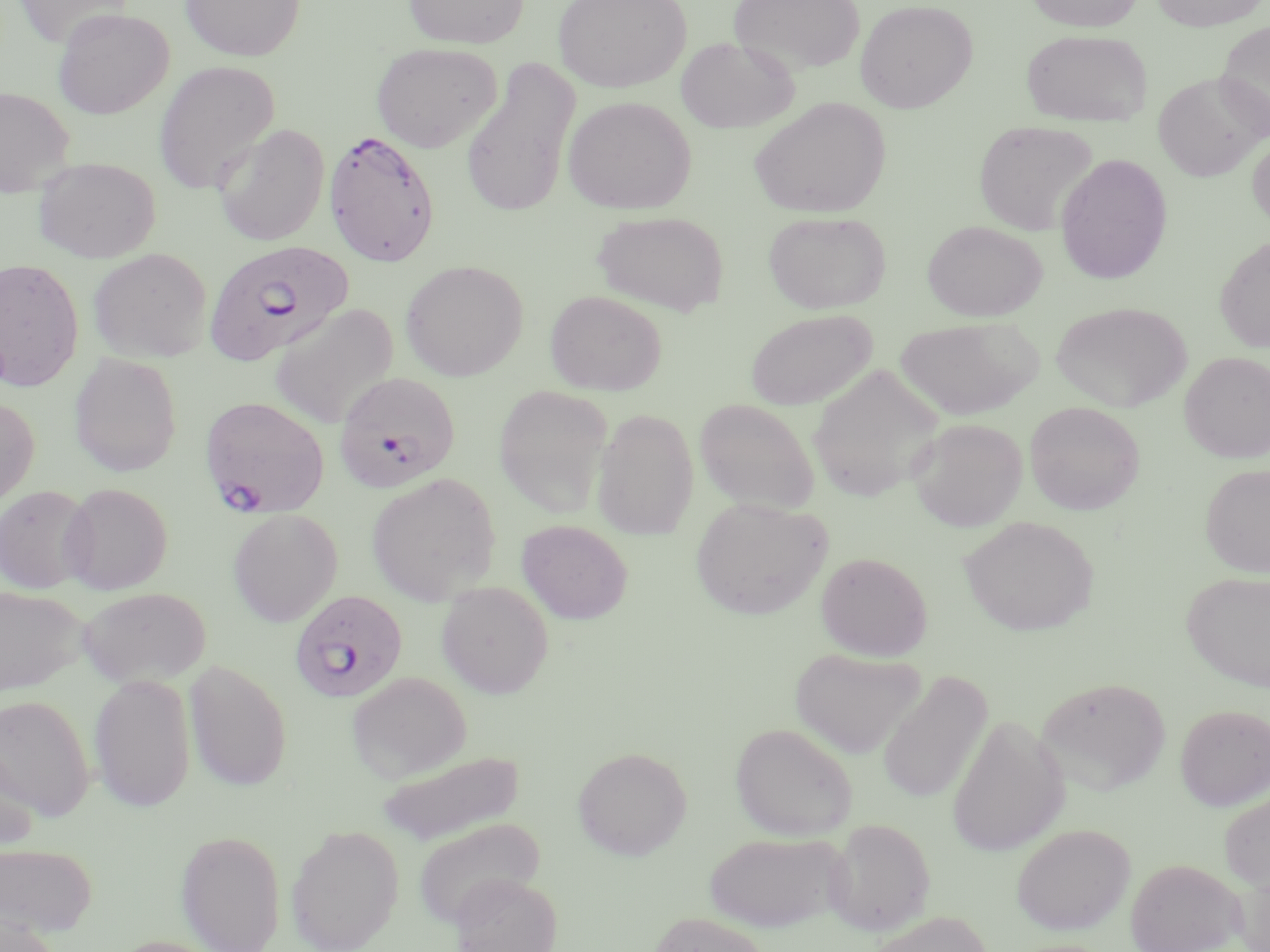

slide_level_diagnosis: Plasmodium falciparum
image_size: 1270×952 pixels
preparation: thin blood smear
uninfected_red_blood_cell_locations_subset: 'approximate bounding boxes as (x1,y1)-(x2,y2) corner pairs in pixels: (180,0)-(306,61), (403,0)-(529,49), (552,0)-(691,93), (728,0)-(865,76), (1024,0)-(1145,32), (1150,0)-(1270,31), (855,1)-(978,113), (14,2)-(132,48), (53,7)-(174,120), (1215,20)-(1270,139), (1021,29)-(1152,127), (676,36)-(799,133), (371,42)-(503,152), (461,57)-(581,218), (153,61)-(280,195), (1152,72)-(1269,182), (0,86)-(75,198), (563,96)-(696,215), (749,96)-(891,218), (974,120)-(1099,236), (213,124)-(330,246), (1248,132)-(1270,233), (1054,154)-(1173,284), (33,156)-(160,263), (592,210)-(729,316), (763,210)-(891,313), (922,220)-(1047,321), (1214,235)-(1270,353), (89,247)-(213,363), (0,258)-(84,391), (400,260)-(528,381), (545,290)-(667,395), (1050,300)-(1192,412), (269,303)-(400,429), (744,308)-(878,411), (895,317)-(1037,420), (1180,351)-(1270,463), (69,353)-(183,477), (808,365)-(944,504), (494,384)-(613,518), (0,395)-(39,509), (694,397)-(820,514), (1025,401)-(1144,515), (592,408)-(699,539), (908,418)-(1028,531), (1200,464)-(1270,576), (366,472)-(501,604), (60,482)-(173,595), (0,484)-(96,593), (691,497)-(832,621), (227,508)-(343,626), (960,516)-(1098,636), (517,520)-(632,624), (815,551)-(933,660), (1181,570)-(1270,691), (436,581)-(554,698), (1,585)-(89,696), (77,586)-(212,688), (789,647)-(925,759), (184,659)-(293,792), (878,668)-(993,806), (348,672)-(471,782), (88,673)-(196,812), (1037,676)-(1171,795), (0,694)-(94,819), (1175,703)-(1270,811), (946,715)-(1068,857), (730,722)-(858,840), (0,743)-(39,854), (572,746)-(692,860), (375,749)-(525,846), (1219,787)-(1270,892), (413,817)-(546,926), (825,818)-(935,935), (1011,822)-(1136,935), (286,824)-(403,952), (176,829)-(286,952), (704,831)-(848,932), (0,841)-(97,938), (1126,858)-(1244,952), (1232,864)-(1270,952), (449,873)-(562,952), (648,911)-(774,952), (866,911)-(993,952), (0,912)-(63,952)'
stain: May-Grünwald-Giemsa
magnification: 1000x
modality: light microscopy
plasmodium_falciparum_infected_red_blood_cell_locations_subset: 'approximate bounding boxes as (x1,y1)-(x2,y2) corner pairs in pixels: (323,129)-(441,267), (334,373)-(460,494), (200,396)-(330,517), (290,589)-(407,703)'
field_of_view: single